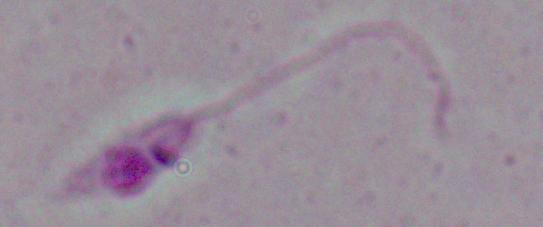
Summary:
  - Magnification: 1000x
  - Modality: photomicrograph
  - Identification: Leishmania